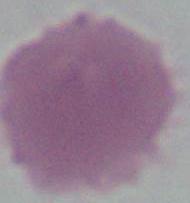

identification = red blood cell
modality = photomicrograph
magnification = 1000x